Report the malaria status of this cell.
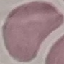

Uninfected.

Summary:
  - Preparation: thin blood film
  - Image type: automatically extracted cell patch, resized to 64 × 64 pixels
  - Stain: Giemsa
  - Capture: smartphone through the microscope eyepiece